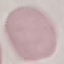 Result: no malaria parasites detected. Automatically extracted cell patch, resized to 64 × 64 pixels. Giemsa stain. Acquired by smartphone through the microscope eyepiece. Thin smear of blood.